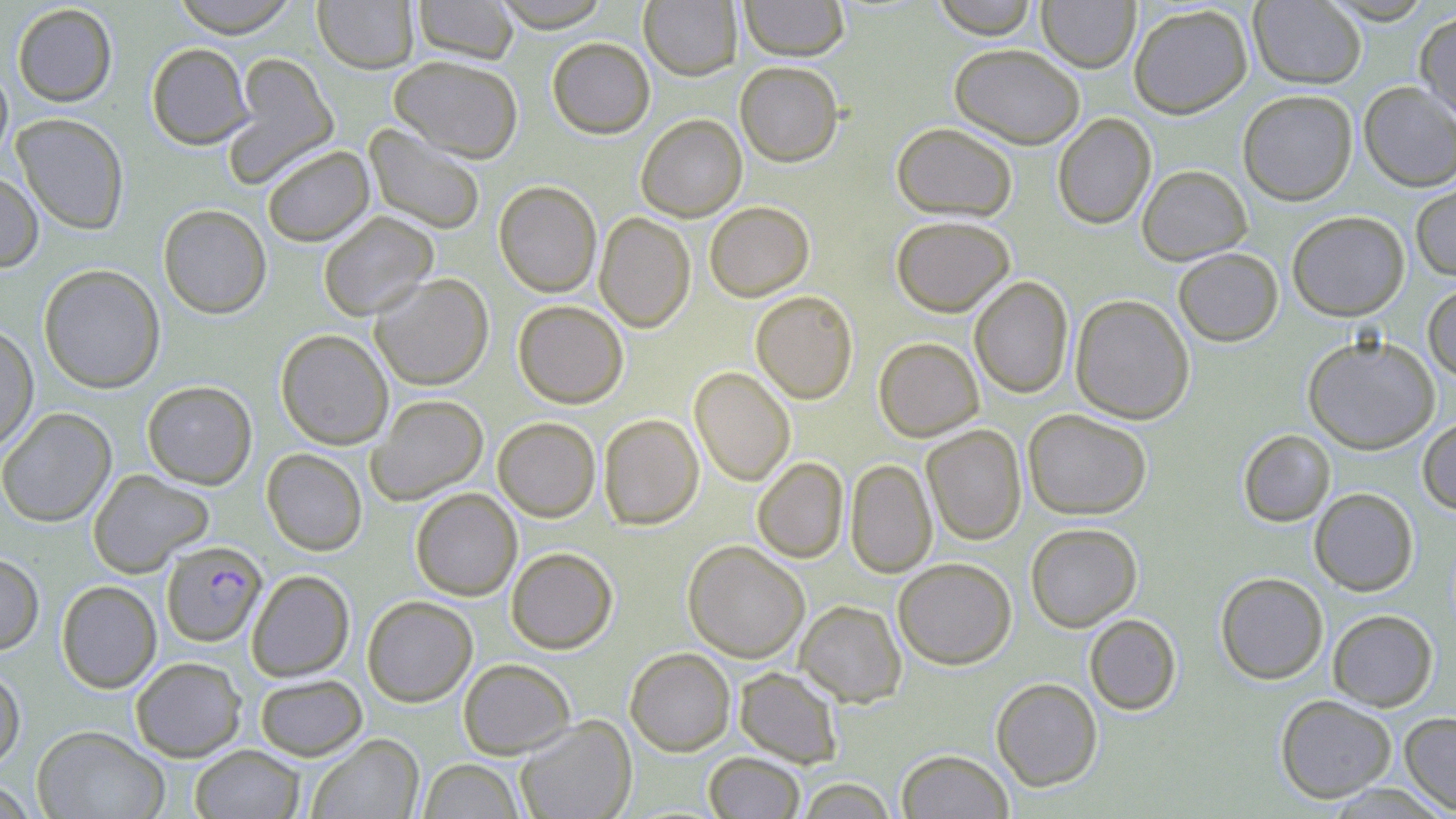
Approximate bounding boxes as named x1/y1/x2/y2 corners in pixels. Plasmodium falciparum-infected red blood cell locations: (x1=162, y1=540, x2=266, y2=646). Uninfected red blood cell locations: (x1=169, y1=0, x2=301, y2=38), (x1=313, y1=0, x2=419, y2=74), (x1=412, y1=0, x2=519, y2=63), (x1=489, y1=0, x2=613, y2=31), (x1=639, y1=0, x2=742, y2=80), (x1=738, y1=0, x2=850, y2=60), (x1=931, y1=0, x2=1040, y2=38), (x1=1319, y1=0, x2=1438, y2=24), (x1=1037, y1=1, x2=1140, y2=72), (x1=1249, y1=1, x2=1366, y2=89), (x1=12, y1=3, x2=118, y2=107), (x1=1128, y1=4, x2=1252, y2=118), (x1=1415, y1=9, x2=1456, y2=124), (x1=547, y1=37, x2=655, y2=138), (x1=146, y1=42, x2=254, y2=149), (x1=949, y1=43, x2=1085, y2=148), (x1=224, y1=53, x2=340, y2=186), (x1=389, y1=55, x2=523, y2=162), (x1=735, y1=61, x2=843, y2=166), (x1=0, y1=64, x2=13, y2=169), (x1=1359, y1=82, x2=1456, y2=191), (x1=1237, y1=89, x2=1358, y2=205), (x1=636, y1=113, x2=747, y2=222), (x1=1052, y1=113, x2=1156, y2=230), (x1=13, y1=114, x2=129, y2=233), (x1=891, y1=122, x2=1017, y2=221), (x1=364, y1=124, x2=486, y2=235), (x1=262, y1=145, x2=374, y2=246), (x1=1137, y1=164, x2=1252, y2=264), (x1=0, y1=170, x2=43, y2=272), (x1=494, y1=180, x2=602, y2=297), (x1=1411, y1=180, x2=1456, y2=281), (x1=705, y1=201, x2=814, y2=301), (x1=158, y1=203, x2=271, y2=318), (x1=1287, y1=210, x2=1409, y2=321), (x1=318, y1=211, x2=438, y2=321), (x1=594, y1=212, x2=695, y2=332), (x1=891, y1=215, x2=1015, y2=316), (x1=1173, y1=247, x2=1283, y2=346), (x1=38, y1=264, x2=165, y2=394), (x1=370, y1=273, x2=494, y2=390), (x1=969, y1=276, x2=1073, y2=399), (x1=1423, y1=281, x2=1456, y2=382), (x1=750, y1=290, x2=858, y2=404), (x1=1070, y1=294, x2=1195, y2=424), (x1=513, y1=300, x2=628, y2=408), (x1=0, y1=323, x2=38, y2=451), (x1=275, y1=329, x2=393, y2=450), (x1=1303, y1=334, x2=1440, y2=454), (x1=873, y1=337, x2=983, y2=441), (x1=690, y1=367, x2=796, y2=486), (x1=142, y1=380, x2=257, y2=489), (x1=368, y1=394, x2=488, y2=504), (x1=0, y1=407, x2=116, y2=527), (x1=1023, y1=409, x2=1152, y2=520), (x1=599, y1=413, x2=704, y2=530), (x1=493, y1=417, x2=601, y2=521), (x1=1417, y1=417, x2=1456, y2=515), (x1=922, y1=425, x2=1026, y2=546), (x1=1238, y1=429, x2=1335, y2=527), (x1=262, y1=449, x2=367, y2=555), (x1=752, y1=457, x2=849, y2=563), (x1=845, y1=459, x2=937, y2=579), (x1=88, y1=469, x2=213, y2=577), (x1=410, y1=488, x2=522, y2=601), (x1=1309, y1=488, x2=1418, y2=596), (x1=1026, y1=523, x2=1142, y2=632), (x1=683, y1=541, x2=810, y2=662), (x1=506, y1=547, x2=618, y2=653), (x1=0, y1=553, x2=44, y2=654), (x1=893, y1=558, x2=1017, y2=669), (x1=247, y1=570, x2=354, y2=681), (x1=1215, y1=572, x2=1328, y2=684), (x1=56, y1=580, x2=162, y2=693), (x1=362, y1=595, x2=477, y2=706), (x1=795, y1=600, x2=907, y2=707), (x1=1327, y1=609, x2=1438, y2=711), (x1=1084, y1=614, x2=1182, y2=715), (x1=625, y1=648, x2=735, y2=755), (x1=130, y1=656, x2=247, y2=762), (x1=458, y1=658, x2=575, y2=758), (x1=0, y1=665, x2=25, y2=771), (x1=734, y1=666, x2=844, y2=769), (x1=254, y1=674, x2=367, y2=760), (x1=990, y1=677, x2=1103, y2=791), (x1=1275, y1=694, x2=1397, y2=803), (x1=1399, y1=711, x2=1456, y2=815), (x1=515, y1=715, x2=637, y2=819), (x1=31, y1=725, x2=170, y2=819), (x1=307, y1=733, x2=424, y2=819), (x1=190, y1=744, x2=305, y2=818), (x1=896, y1=749, x2=1013, y2=819), (x1=703, y1=752, x2=805, y2=818), (x1=418, y1=759, x2=524, y2=819), (x1=795, y1=778, x2=899, y2=819), (x1=0, y1=780, x2=38, y2=818). Slide-level diagnosis: Plasmodium falciparum. Image is 1456×819 pixels. May-Grünwald-Giemsa stain. One field of a larger specimen. Light microscopy. Captured at 1000x magnification. Thin blood smear.